Assess this cell for malaria.
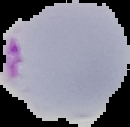
Parasitized.

Summary:
  - Image type: cell region segmented out of the field of view; surrounding area masked to black
  - Image size: 130×127 pixels
  - Preparation: thin blood smear